Classify this cell by malaria status.
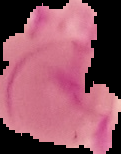
Uninfected.

preparation: thin blood film
image_type: segmented cell region with the area outside set to black
image_size: 121×154 pixels